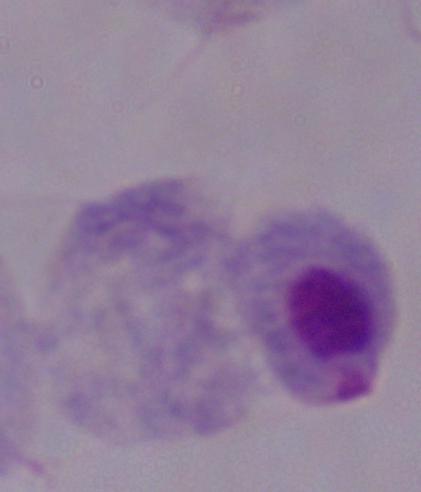
Summary:
  - Identification: trichomonad
  - Magnification: 1000x
  - Modality: micrograph